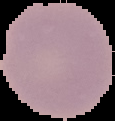

Summary:
  - Result: negative for Plasmodium parasites
  - Preparation: thin blood film
  - Image size: 115×121 pixels
  - Image type: cell region segmented out of the field of view; surrounding area masked to black